Give the preparation type.
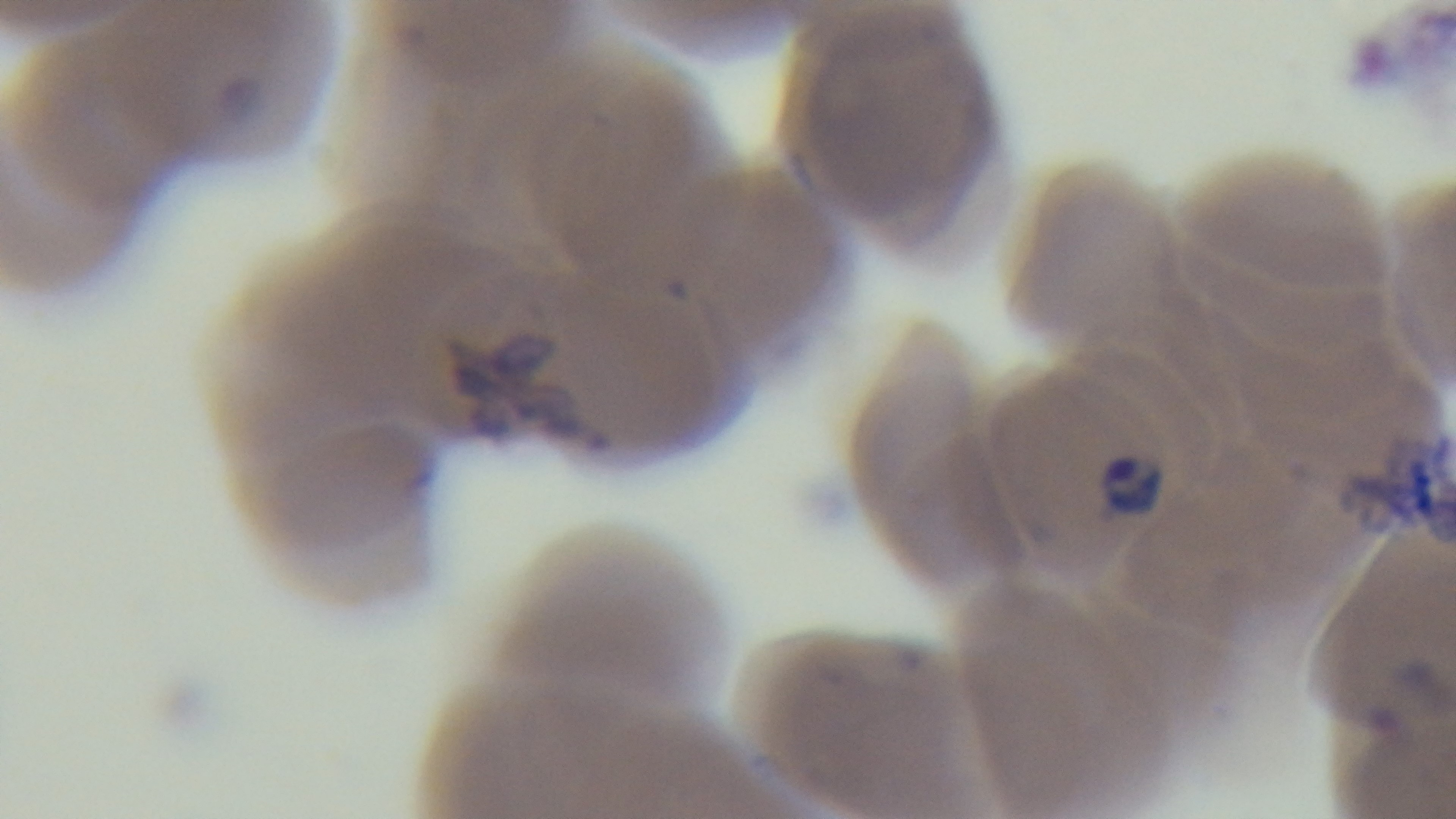

A thin smear.

field of view = single
stain = Giemsa
capture = mounted 4K digital camera
objective = 100x oil immersion
malaria status = positive
modality = light microscopy